Name the blood parasite species.
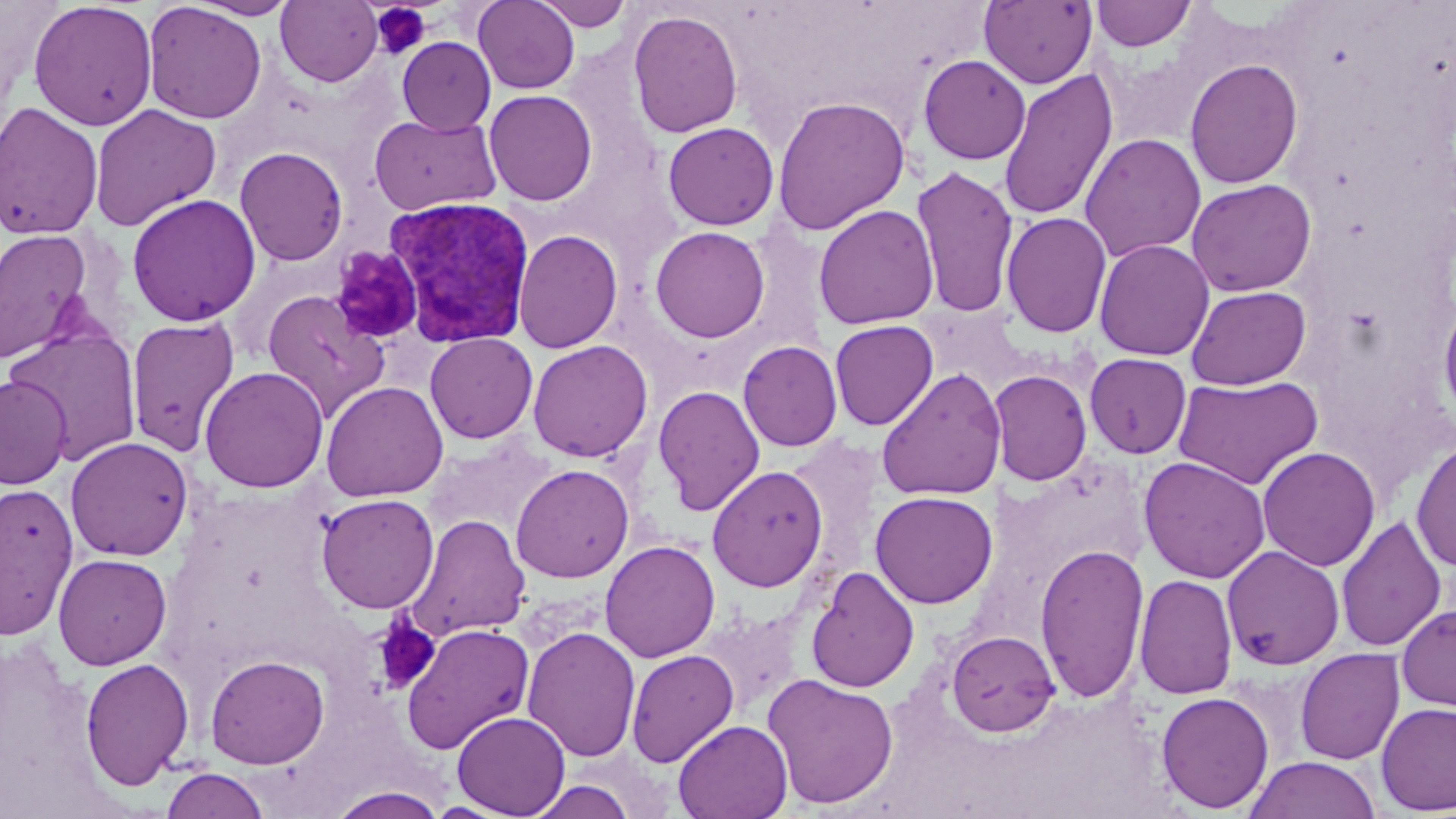

Plasmodium vivax.

Summary:
  - Coordinate format: approximate bounding boxes as [x1, y1, x2, y2] in pixels
  - Uninfected red blood cell locations: [188, 0, 300, 20], [276, 0, 382, 87], [473, 0, 581, 94], [531, 0, 633, 31], [979, 0, 1097, 89], [1091, 0, 1196, 51], [28, 1, 158, 131], [143, 2, 266, 124], [627, 9, 744, 139], [397, 36, 496, 135], [918, 54, 1031, 164], [1184, 58, 1303, 188], [997, 68, 1118, 221], [484, 89, 597, 206], [771, 95, 911, 236], [0, 101, 104, 240], [89, 104, 221, 232], [369, 114, 502, 215], [662, 122, 780, 231], [1079, 132, 1206, 262], [235, 146, 348, 266], [911, 165, 1019, 320], [1186, 178, 1317, 296], [127, 193, 261, 326], [813, 204, 939, 329], [1001, 211, 1112, 338], [650, 225, 770, 343], [0, 228, 96, 365], [513, 229, 623, 354], [1093, 238, 1214, 361], [1186, 285, 1311, 390], [262, 290, 389, 421], [1437, 294, 1456, 428], [125, 316, 240, 458], [829, 319, 938, 430], [6, 326, 143, 464], [424, 332, 538, 444], [527, 339, 653, 462], [738, 340, 842, 451], [1084, 352, 1192, 458], [199, 366, 329, 492], [876, 368, 1007, 501], [988, 369, 1092, 486], [1172, 374, 1324, 490], [0, 375, 72, 489], [321, 380, 448, 502], [653, 385, 765, 516], [65, 436, 193, 561], [1411, 436, 1456, 572], [1257, 446, 1380, 572], [1138, 455, 1271, 583], [510, 463, 634, 583], [707, 464, 829, 592], [0, 482, 78, 638], [870, 490, 998, 608], [315, 493, 439, 614], [405, 513, 531, 642], [1336, 515, 1447, 653], [600, 540, 721, 663], [1035, 542, 1148, 704], [1221, 545, 1345, 669], [53, 553, 172, 670], [66, 553, 178, 788], [805, 566, 920, 693], [1134, 573, 1238, 700], [1396, 603, 1456, 712], [400, 621, 535, 755], [522, 626, 641, 762], [946, 629, 1061, 737], [1295, 647, 1405, 765], [625, 648, 739, 768], [205, 654, 330, 769], [80, 657, 195, 790], [762, 673, 899, 809], [1155, 691, 1274, 813], [1376, 702, 1456, 815], [452, 711, 570, 818], [673, 719, 793, 819], [1244, 755, 1381, 819], [161, 767, 271, 819], [523, 779, 637, 819], [326, 786, 450, 819]
  - Platelet locations: [371, 3, 431, 61], [329, 247, 424, 345], [372, 616, 441, 694]
  - Plasmodium vivax-infected red blood cell locations: [383, 196, 535, 348]
  - Stain: May-Grünwald-Giemsa
  - Magnification: 1000x
  - Image size: 1456×819 pixels
  - Preparation: thin blood smear
  - Modality: light microscopy
  - Field of view: single